Assess the morphology of the erythrocytes.
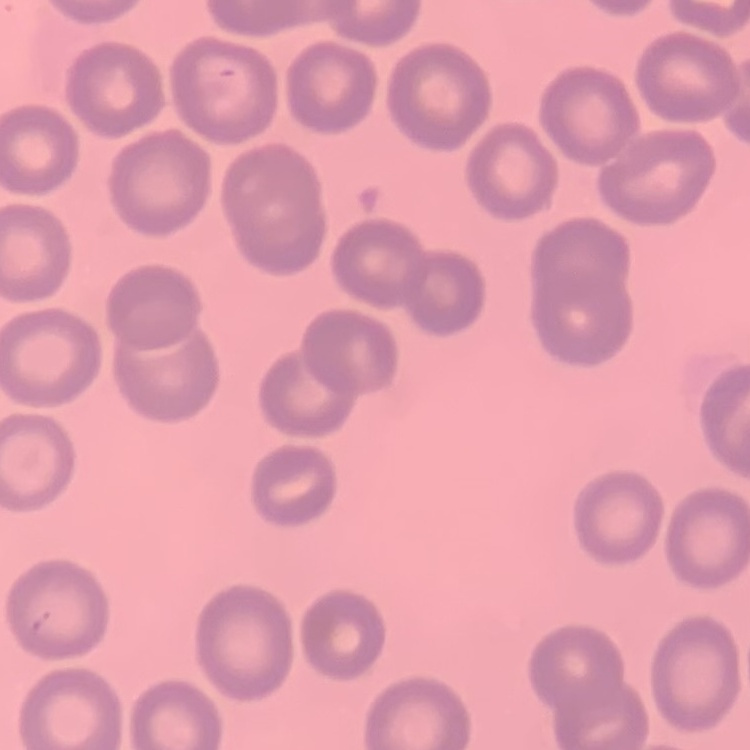
No rouleaux formation.

preparation = thin blood smear
stain = Field's or Giemsa
image type = square crop of a larger photomicrograph